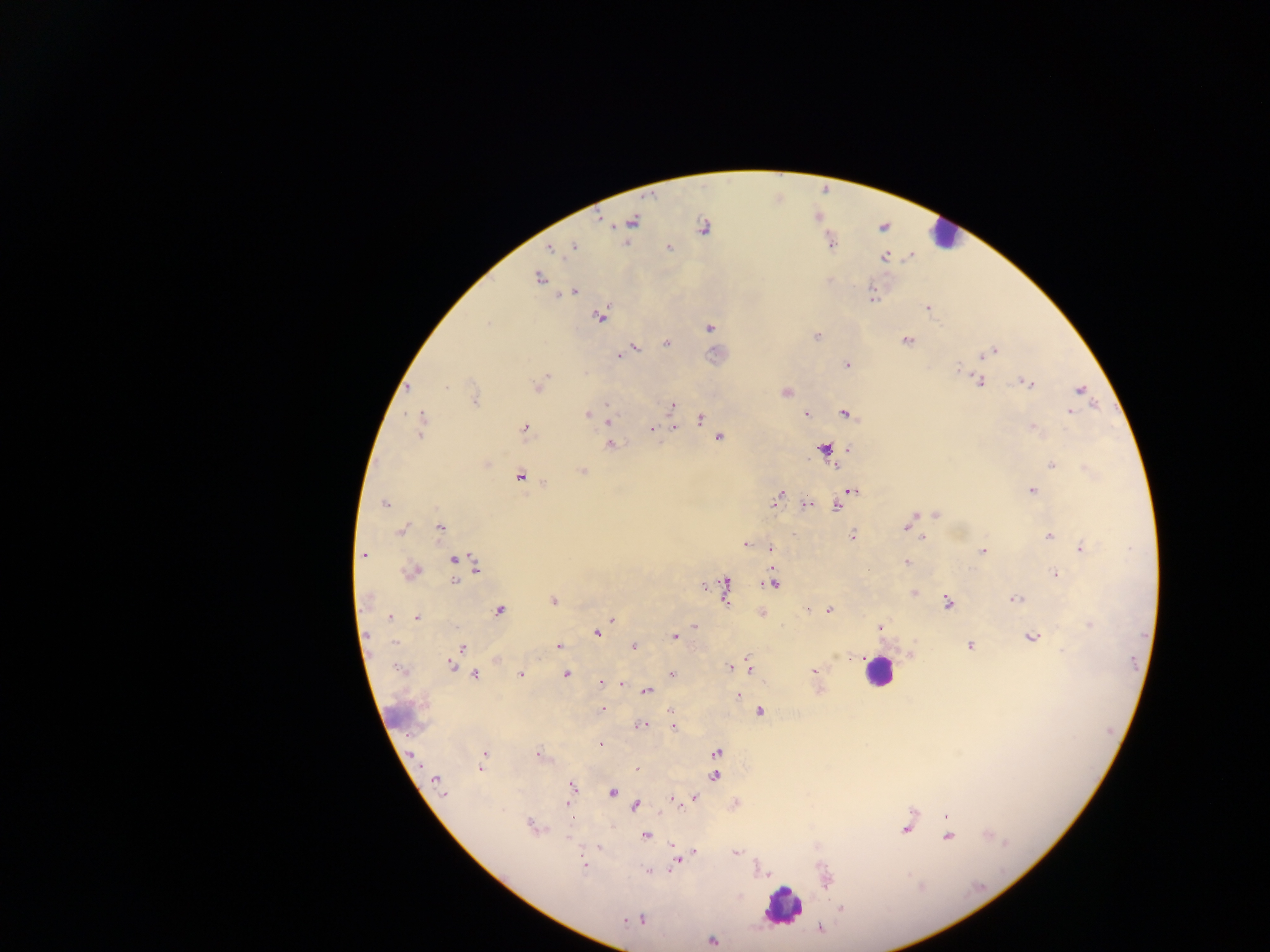

{
  "preparation": "thick blood smear",
  "field_of_view": "single",
  "leukocyte_locations": "approximate centers as x y in pixels: 946 230; 873 677; 778 908",
  "country": "Ghana",
  "plasmodium_parasite_locations": "approximate centers as x y in pixels: 613 226; 703 228; 574 247; 549 249; 670 250; 538 277; 574 290; 926 308; 599 317; 488 324; 709 327; 817 336; 907 340; 666 343; 635 348; 995 350; 619 356; 847 365; 958 368; 545 378; 978 380; 1025 381; 448 387; 538 387; 1080 390; 607 405; 671 406; 1070 410; 845 414; 586 415; 805 415; 700 418; 421 420; 607 421; 673 426; 524 429; 653 430; 719 437; 610 445; 824 448; 847 448; 1052 464; 582 471; 520 475; 1033 489; 850 490; 780 494; 774 500; 384 503; 806 504; 837 507; 914 513; 936 513; 401 528; 905 528; 439 529; 400 531; 853 533; 925 535; 1048 535; 744 544; 1082 548; 772 549; 982 550; 363 557; 453 559; 908 561; 475 565; 415 570; 1055 574; 455 582; 773 584; 703 585; 726 587; 1013 598; 365 599; 553 600; 947 602; 805 609; 830 610; 500 611; 417 616; 391 618; 613 619; 694 625; 879 626; 605 627; 597 633; 367 634; 673 637; 1030 638; 394 641; 559 646; 633 646; 972 646; 464 647; 847 656; 838 657; 496 662; 451 664; 729 667; 749 667; 814 671; 476 673; 519 673; 671 673; 565 674; 599 682; 623 686; 820 690; 647 693; 738 696; 602 709; 668 710; 759 711; 641 724; 673 725; 672 727; 600 743; 488 751; 718 753; 414 754; 538 754; 639 768; 480 769; 715 776; 435 779; 571 785; 613 792; 444 795; 694 797; 672 798; 567 804; 637 805; 912 811; 946 815; 573 821; 529 822; 904 830; 645 836; 569 838; 599 848; 736 852; 675 859; 583 864; 646 869; 842 908; 642 921; 711 940",
  "image_size": "1270×952 pixels",
  "capture": "mobile-phone photograph through a microscope"
}